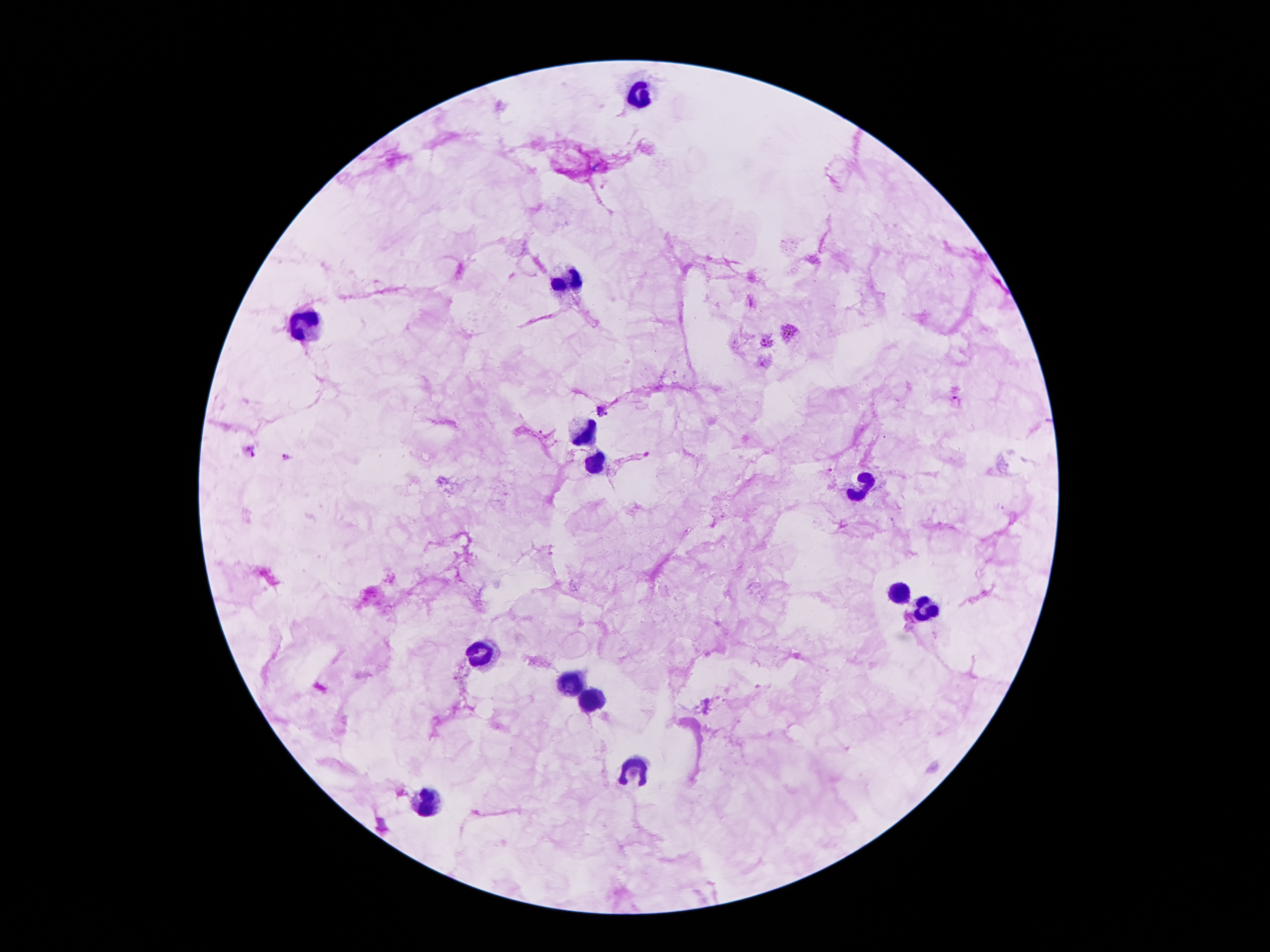

Approximate centers as [x, y] in pixels.
Summary:
  - Leukocyte locations: [634, 93], [563, 283], [305, 327], [576, 431], [599, 464], [854, 485], [896, 587], [935, 606], [476, 650], [566, 686], [596, 699], [634, 776], [428, 802]
  - Malaria parasite locations: [790, 333], [767, 341], [957, 400], [601, 410], [250, 451], [287, 455], [830, 469]
  - Preparation: thick blood smear
  - Image size: 1270×952 pixels
  - Patient malaria status: positive for Plasmodium falciparum
  - Magnification: 100x
  - Field of view: single
  - Stain: Giemsa
  - Capture: smartphone through the microscope eyepiece